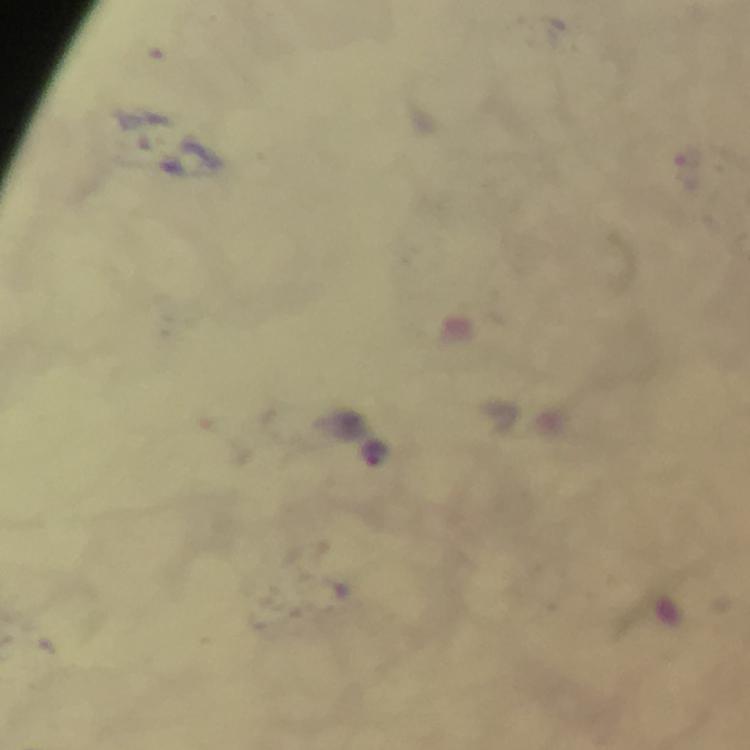 Approximate object centers, in pixels from the top-left corner. Malaria parasite locations: (x=690, y=156), (x=374, y=454). Cropped region of a single field of view. Giemsa-stained preparation. Photographed through the microscope with a smartphone camera. Thick blood film. Immersion oil applied. At 100x magnification. From a diagnostic examination for malaria. Image is 750×750 pixels.